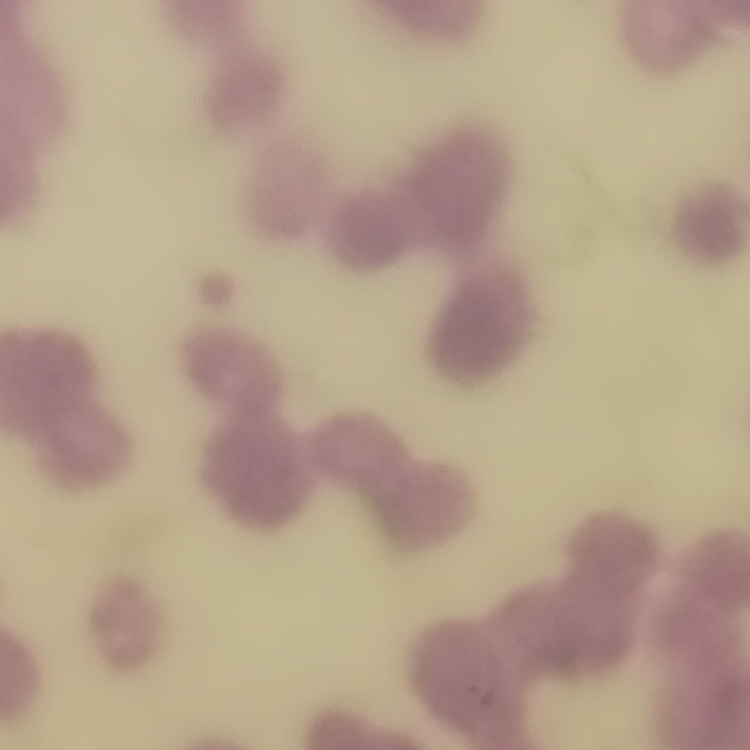 The erythrocytes show rouleaux formation. Thin peripheral smear. Square crop of a larger photomicrograph. Field's or Giemsa stain.